Classify this cell by malaria status.
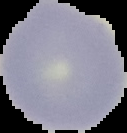
It is uninfected.

Summary:
  - Image type: segmented cell region on a black background
  - Image size: 127×133 pixels
  - Preparation: thin blood smear